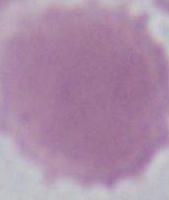
Summary:
  - Identification: red blood cell
  - Modality: micrograph
  - Magnification: 1000x